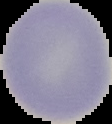

{
  "image_size": "112×124 pixels",
  "malaria_status": "uninfected",
  "image_type": "cell region segmented out of the field of view; surrounding area masked to black",
  "preparation": "thin blood film"
}